Give the extent of all uninfected red blood cells.
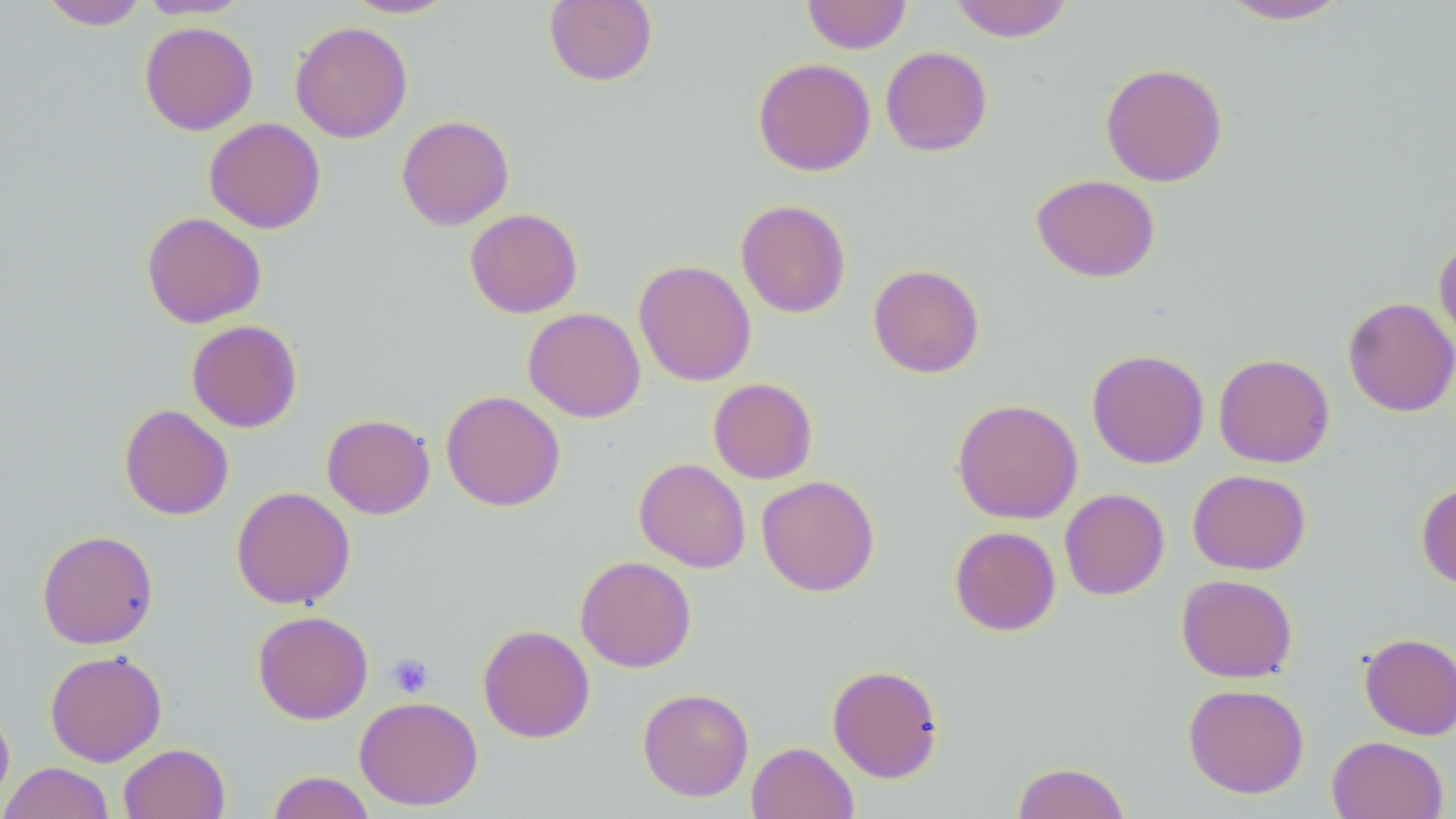
Approximate bounding boxes as [x1, y1, x2, y2] in pixels.
Uninfected red blood cells: [40, 0, 148, 30], [139, 0, 250, 19], [343, 0, 459, 19], [543, 0, 658, 87], [802, 0, 912, 54], [948, 0, 1074, 42], [1216, 0, 1353, 25], [139, 21, 258, 135], [289, 21, 413, 143], [880, 46, 993, 156], [752, 57, 876, 176], [1100, 62, 1228, 187], [396, 115, 514, 231], [204, 118, 326, 234], [1031, 173, 1160, 282], [735, 199, 851, 318], [465, 208, 583, 318], [141, 211, 267, 328], [1434, 235, 1456, 349], [634, 260, 757, 386], [868, 264, 985, 379], [1343, 297, 1456, 417], [523, 307, 646, 422], [186, 320, 302, 433], [1087, 349, 1209, 468], [1214, 353, 1335, 468], [708, 378, 818, 484], [441, 390, 565, 511], [951, 398, 1083, 524], [119, 404, 234, 520], [321, 413, 435, 519], [634, 457, 751, 573], [1188, 469, 1312, 575], [756, 475, 880, 596], [1416, 481, 1456, 590], [231, 486, 356, 609], [1059, 488, 1170, 600], [949, 526, 1061, 636], [36, 529, 159, 649], [575, 555, 696, 672], [1176, 573, 1298, 683], [252, 610, 373, 724], [477, 624, 595, 743], [1358, 632, 1456, 740], [45, 649, 167, 766], [826, 664, 944, 783], [1183, 683, 1309, 798], [638, 687, 754, 801], [353, 695, 483, 811], [0, 706, 14, 810], [1326, 735, 1449, 819], [746, 741, 859, 819], [118, 743, 230, 819], [1011, 761, 1130, 819], [0, 762, 116, 819], [267, 770, 376, 819].

slide-level diagnosis = no evidence of blood parasites
preparation = thin blood film
stain = May-Grünwald-Giemsa
magnification = 1000x
modality = light microscopy
platelet locations = approximate bounding boxes as [x1, y1, x2, y2] in pixels: [386, 653, 434, 698]
field of view = one of a larger specimen
image size = 1456×819 pixels